Give the position of every Plasmodium parasite.
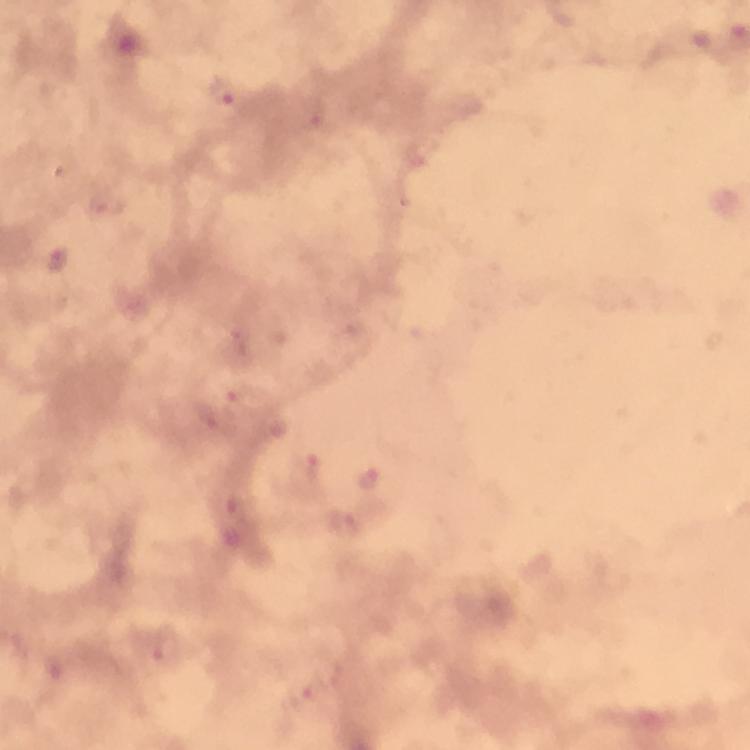

Approximate object centers, in pixels from the top-left corner.
Plasmodium parasites: (x=224, y=92), (x=241, y=396), (x=307, y=473), (x=368, y=478), (x=347, y=525), (x=165, y=647), (x=302, y=695).

{
  "preparation": "thick smear",
  "cropped_from": "one field of view",
  "magnification": "100x",
  "immersion_oil": "used",
  "context": "from a diagnostic examination for malaria",
  "capture": "smartphone photograph through a microscope",
  "image_size": "750×750 pixels",
  "stain": "Giemsa"
}